Identify the parasite.
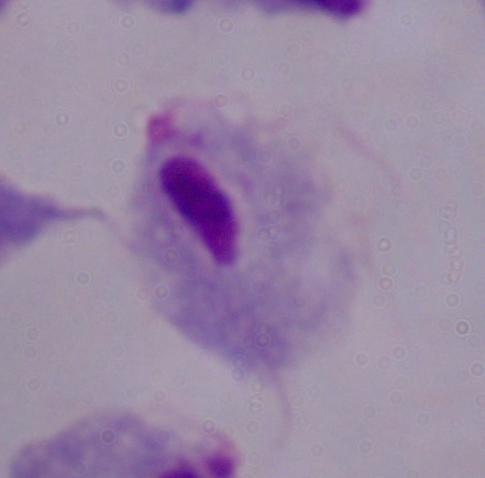
A trichomonad.

Summary:
  - Modality: photomicrograph
  - Magnification: 1000x